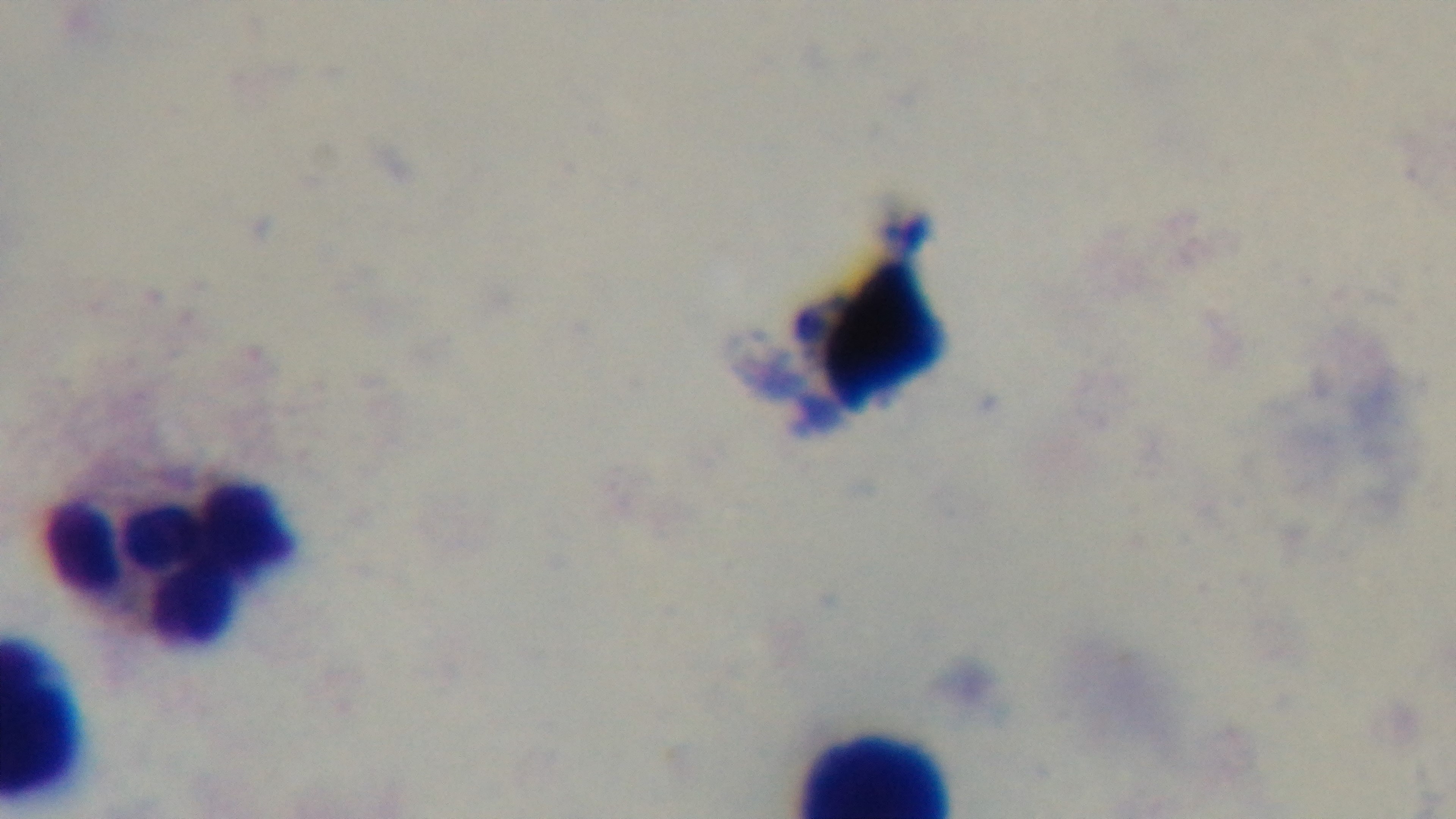 Oil-immersion objective, 100x. Single field of view. Preparation: thick. Mounted 4K digital camera. Malaria status: negative. Giemsa stain. Light microscopy.